Describe the morphology of the erythrocytes.
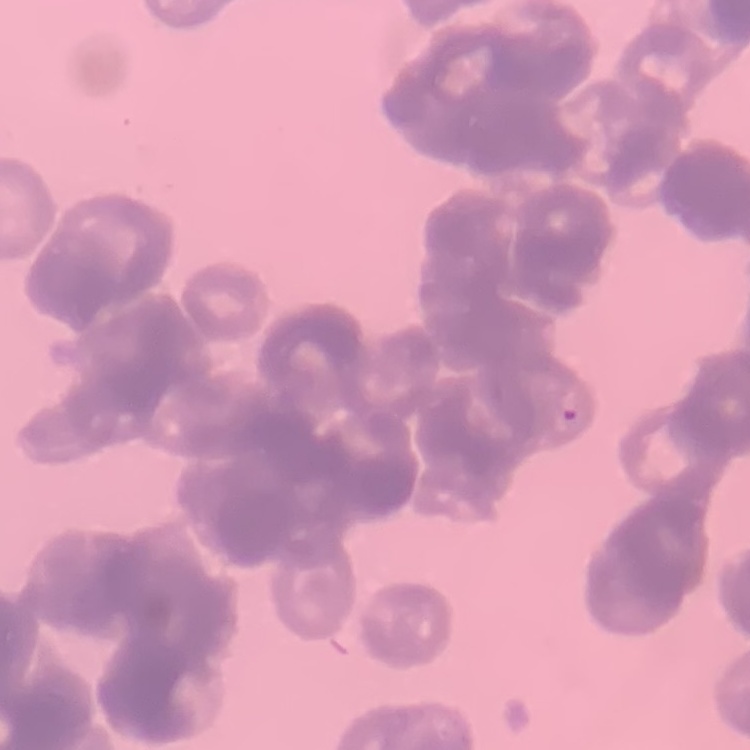
They show rouleaux formation.

Field's or Giemsa stain. Thin blood film. Square crop of a larger photomicrograph.